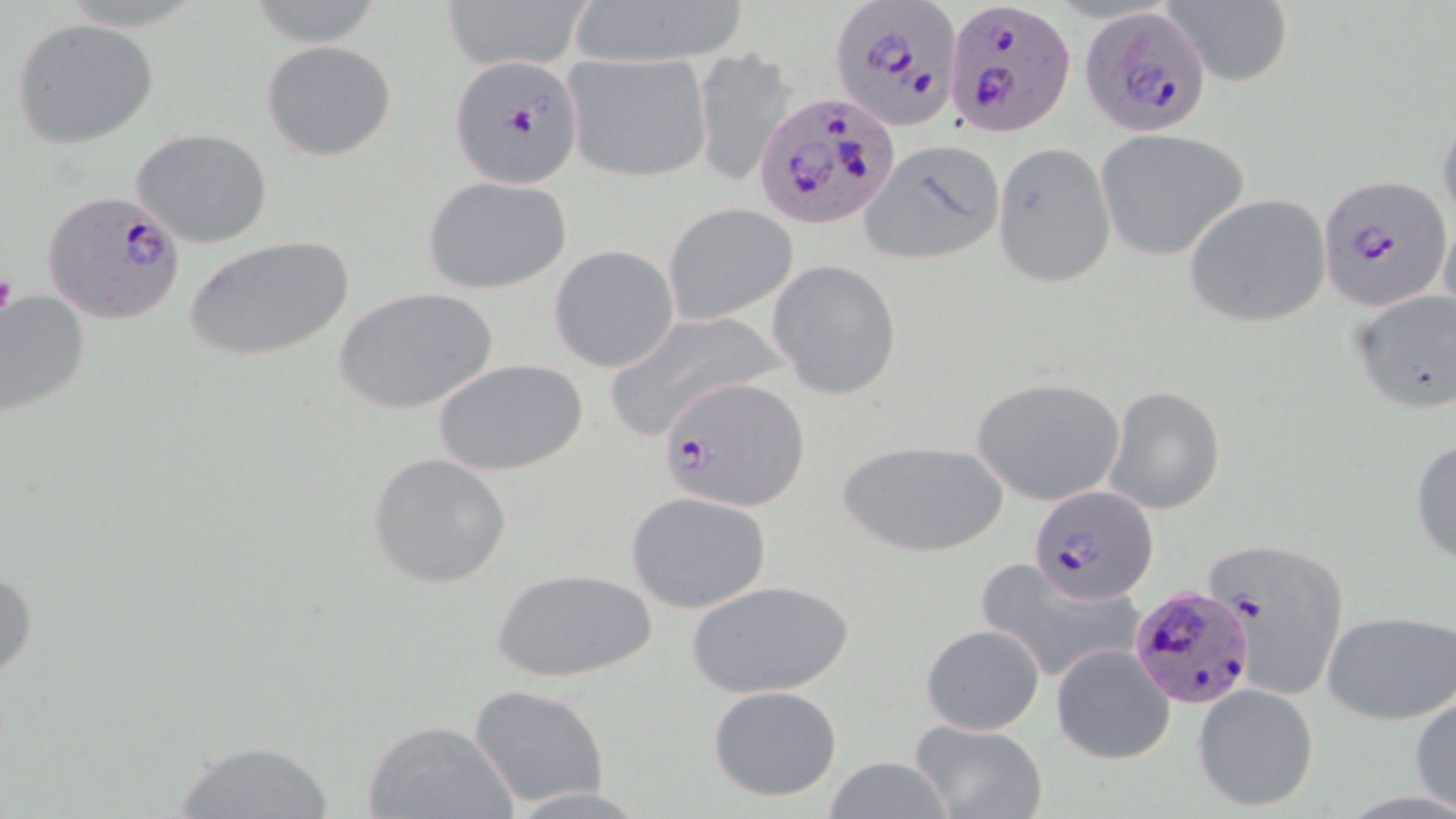
Summary:
  - Coordinate format: approximate bounding boxes as [x1, y1, x2, y2] in pixels
  - Plasmodium falciparum-infected red blood cell locations: [830, 0, 960, 131], [944, 2, 1074, 140], [1081, 4, 1215, 137], [448, 55, 584, 186], [754, 90, 898, 228], [1318, 173, 1452, 312], [42, 189, 187, 325], [662, 375, 808, 512], [1029, 484, 1160, 605], [1127, 583, 1258, 712]
  - Uninfected red blood cell locations: [439, 0, 596, 71], [563, 0, 753, 69], [1164, 0, 1293, 88], [243, 1, 390, 48], [11, 17, 159, 148], [261, 39, 396, 162], [692, 48, 798, 188], [561, 52, 713, 183], [1436, 109, 1456, 236], [133, 128, 273, 247], [1096, 129, 1249, 261], [861, 140, 1003, 265], [992, 141, 1115, 288], [422, 175, 574, 294], [1182, 193, 1332, 328], [663, 202, 799, 324], [184, 235, 354, 363], [549, 244, 681, 373], [768, 259, 903, 399], [335, 285, 498, 415], [1350, 288, 1456, 415], [0, 291, 89, 419], [603, 308, 785, 439], [434, 357, 589, 477], [970, 376, 1126, 505], [1104, 387, 1226, 514], [1410, 436, 1456, 566], [836, 437, 1006, 559], [369, 453, 513, 588], [626, 490, 772, 613], [1200, 535, 1351, 706], [973, 558, 1144, 688], [0, 559, 38, 681], [492, 566, 655, 682], [686, 577, 856, 700], [1320, 610, 1456, 725], [920, 623, 1045, 735], [1050, 642, 1175, 765], [469, 682, 609, 808], [1192, 682, 1320, 812], [708, 684, 843, 800], [1411, 691, 1456, 813], [363, 718, 519, 819], [907, 719, 1047, 819], [168, 739, 338, 819], [822, 755, 953, 819], [503, 786, 658, 817]
  - Platelet locations: [0, 270, 18, 323]
  - Slide-level diagnosis: Plasmodium falciparum
  - Stain: May-Grünwald-Giemsa
  - Field of view: one of a larger specimen
  - Modality: light microscopy
  - Image size: 1456×819 pixels
  - Magnification: 1000x
  - Preparation: thin blood smear